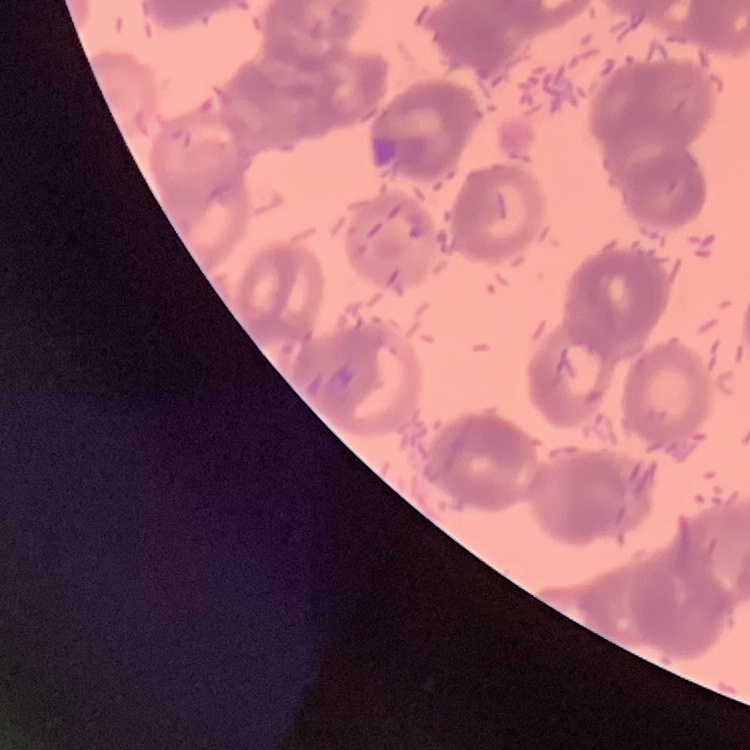

red_blood_cell_morphology: rouleaux formation
stain: Field's or Giemsa
preparation: thin peripheral smear
image_type: one tile cut from a larger photomicrograph